Classify this cell by malaria status.
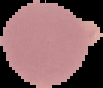

It is uninfected.

Summary:
  - Preparation: thin blood film
  - Image size: 103×88 pixels
  - Image type: segmented cell region on a black background